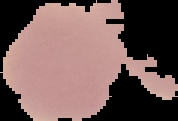

Summary:
  - Preparation: thin blood film
  - Image type: cell region segmented out of the field of view; surrounding area masked to black
  - Image size: 178×121 pixels
  - Result: no Plasmodium parasites seen